Give the preparation type.
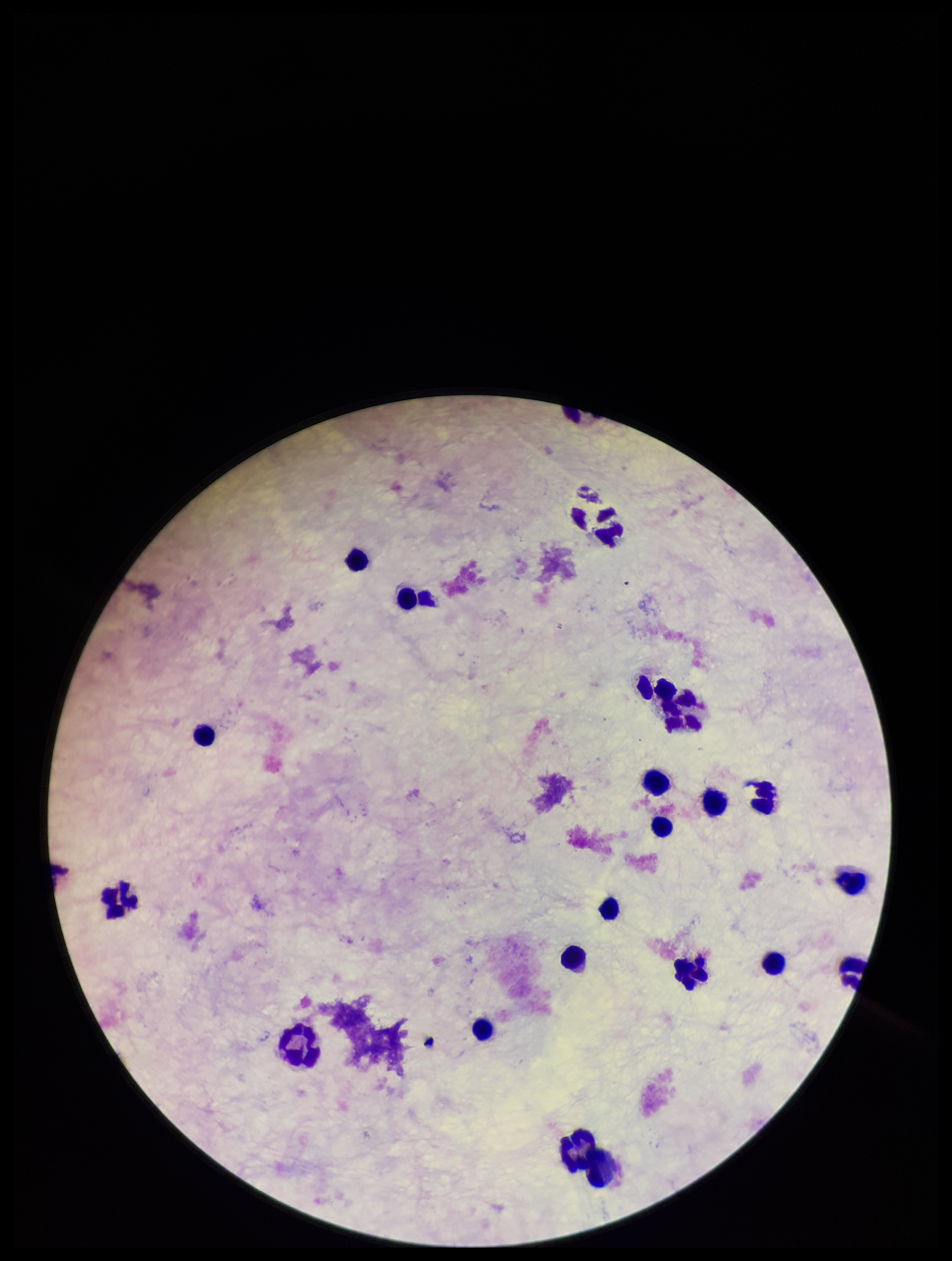

A thick smear.

Summary:
  - Patient malaria status: negative
  - Parasite count: 0
  - Image size: 952×1261 pixels
  - Capture: smartphone photograph through the microscope eyepiece
  - Leukocyte count: 20
  - Stain: Giemsa
  - Plasmodium parasites: none seen
  - Field of view: one from this slide